Point out each Plasmodium parasite.
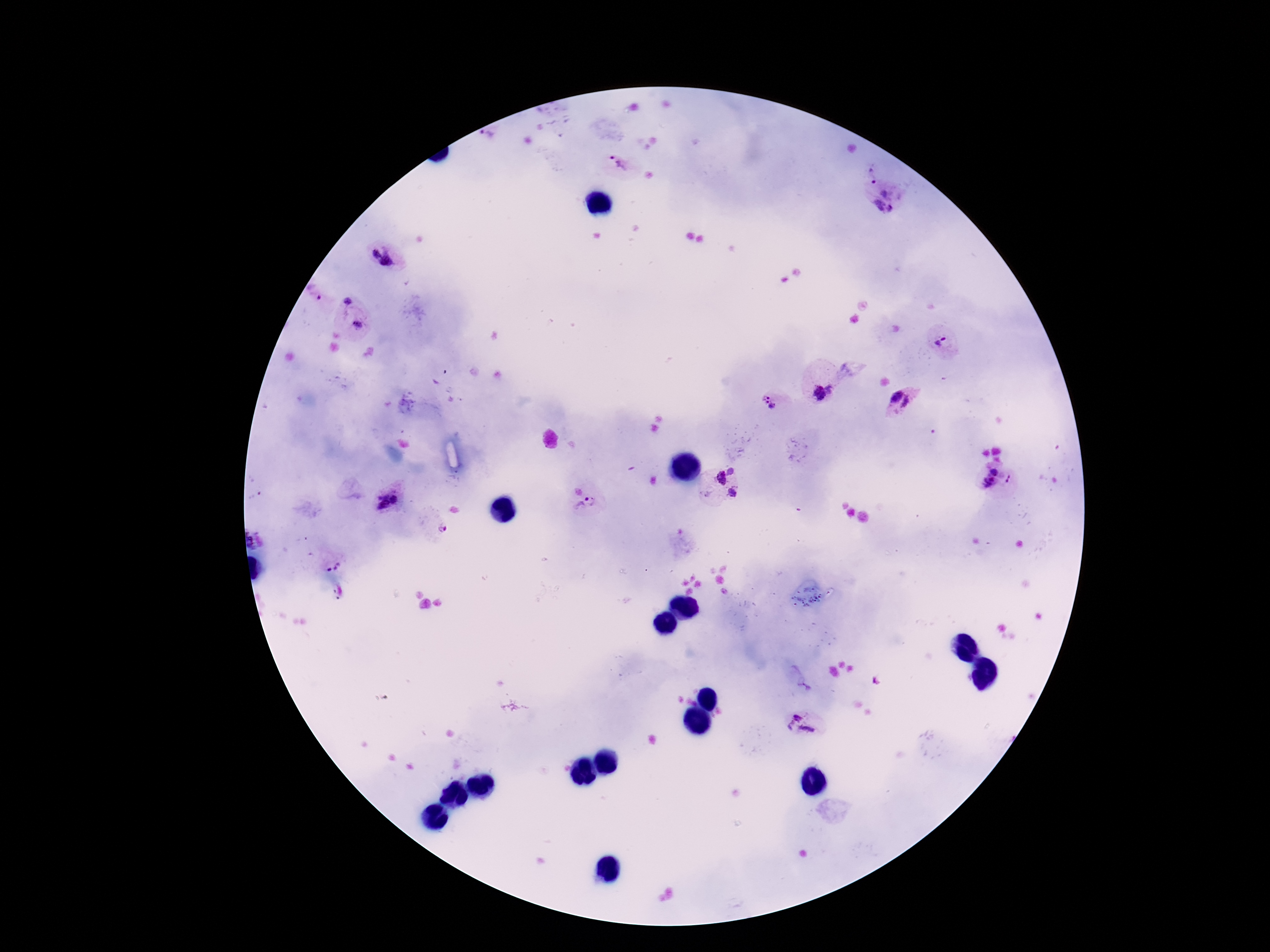
Approximate centers as (x, y) in pixels.
Plasmodium parasites: (488, 135), (618, 164), (872, 176), (885, 193), (878, 205), (889, 208), (381, 256), (319, 298), (347, 301), (358, 325), (943, 343), (829, 389), (820, 393), (893, 395), (768, 403), (910, 403), (996, 470), (731, 471), (721, 478), (1008, 479), (988, 482), (732, 494), (395, 499), (380, 501), (585, 505), (443, 528), (334, 566), (798, 715), (790, 725), (806, 731).

Giemsa-stained preparation. Single field of view. 100x magnification. Patient malaria status: infected. Photographed through the microscope eyepiece with a smartphone camera. Image is 1270×952 pixels. Thick blood smear.